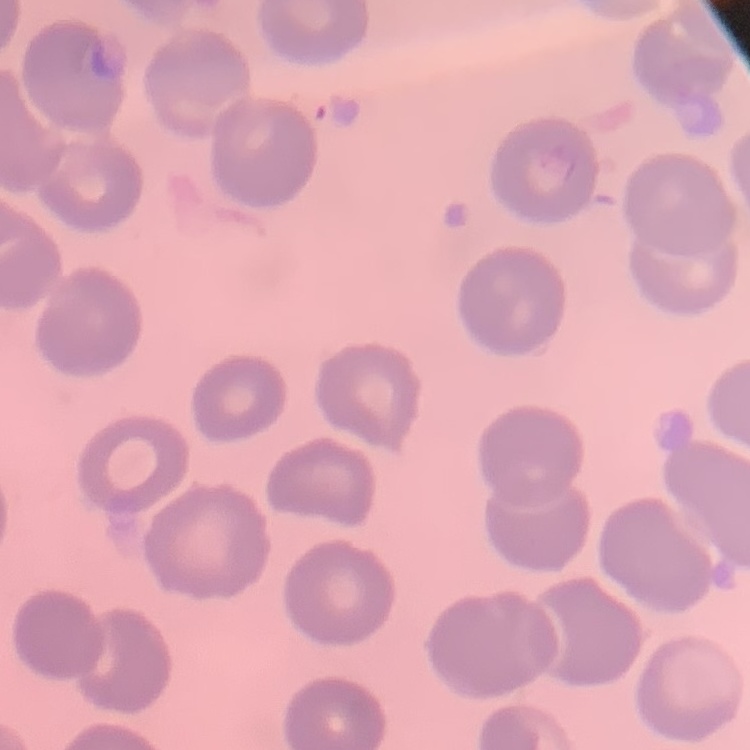

Summary:
  - Red blood cell morphology: no rouleaux formation
  - Stain: Field's or Giemsa
  - Preparation: thin blood smear
  - Image type: one tile cut from a larger photomicrograph